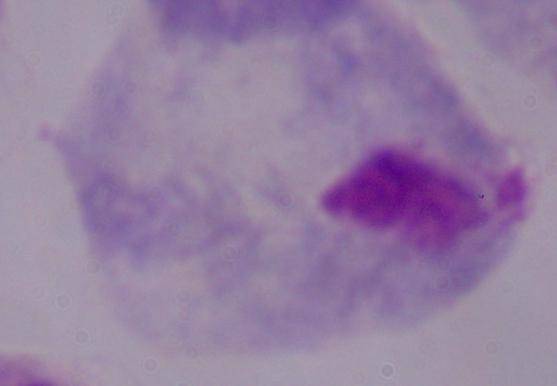
magnification = 1000x
identification = trichomonad
modality = photomicrograph